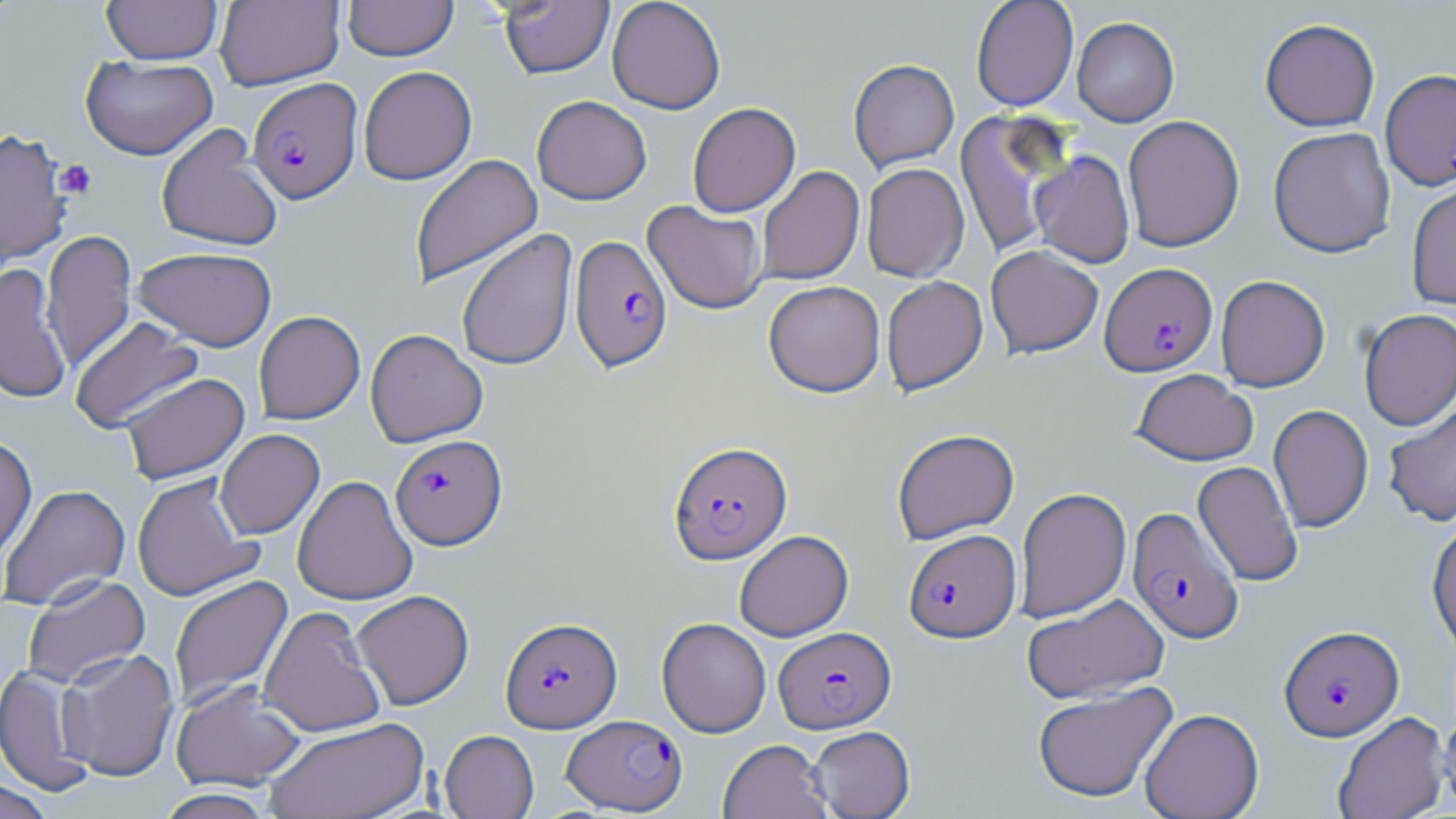

Summary:
  - Coordinate format: approximate bounding boxes as (x1,y1)-(x2,y2) corner pairs in pixels
  - Uninfected red blood cell locations: (0,0)-(25,28), (102,0)-(222,64), (215,0)-(344,90), (343,0)-(458,61), (607,0)-(726,114), (970,0)-(1079,112), (500,1)-(614,79), (1072,17)-(1179,127), (1259,18)-(1380,131), (80,54)-(218,160), (848,58)-(959,172), (358,66)-(477,185), (532,95)-(651,204), (687,102)-(800,217), (955,110)-(1073,260), (1122,115)-(1245,252), (156,123)-(283,252), (1268,127)-(1396,258), (0,128)-(72,266), (1030,151)-(1135,268), (409,153)-(543,288), (861,163)-(969,282), (756,166)-(864,285), (1406,180)-(1456,310), (643,200)-(768,315), (41,229)-(137,372), (457,229)-(578,372), (985,245)-(1104,359), (133,246)-(277,350), (0,263)-(72,404), (1215,275)-(1330,392), (881,276)-(988,396), (763,280)-(886,397), (1358,308)-(1456,430), (253,311)-(365,424), (69,316)-(204,433), (365,328)-(488,447), (1131,369)-(1258,466), (119,373)-(250,484), (1382,400)-(1456,527), (1268,404)-(1373,534), (891,428)-(1020,544), (215,429)-(325,539), (0,436)-(37,562), (1192,460)-(1304,587), (131,473)-(262,602), (292,475)-(417,605), (0,484)-(130,612), (1015,487)-(1132,623), (1426,520)-(1456,659), (734,530)-(854,642), (22,574)-(151,691), (168,575)-(293,710), (351,590)-(474,710), (1021,594)-(1171,705), (259,605)-(386,737), (656,617)-(771,737), (57,647)-(180,781), (1,664)-(95,797), (170,679)-(307,792), (1032,682)-(1178,804), (1140,708)-(1264,819), (1438,711)-(1456,816), (1332,712)-(1450,819), (264,717)-(430,818), (808,726)-(915,819), (439,730)-(539,819), (718,739)-(831,819), (0,780)-(54,818), (155,788)-(276,819)
  - Plasmodium falciparum-infected red blood cell locations: (1380,68)-(1456,190), (247,77)-(362,205), (569,235)-(673,373), (1099,262)-(1217,377), (390,434)-(507,549), (668,441)-(792,565), (1126,507)-(1245,644), (903,529)-(1021,643), (500,617)-(622,732), (1279,624)-(1404,741), (774,626)-(895,733), (561,714)-(687,815)
  - Platelet locations: (53,159)-(97,198)
  - Slide-level diagnosis: Plasmodium falciparum
  - Stain: May-Grünwald-Giemsa
  - Field of view: single
  - Preparation: thin blood film
  - Magnification: 1000x
  - Image size: 1456×819 pixels
  - Modality: light microscopy